Name the parasite shown.
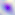
Toxoplasma gondii.

Micrograph. 400x magnification.